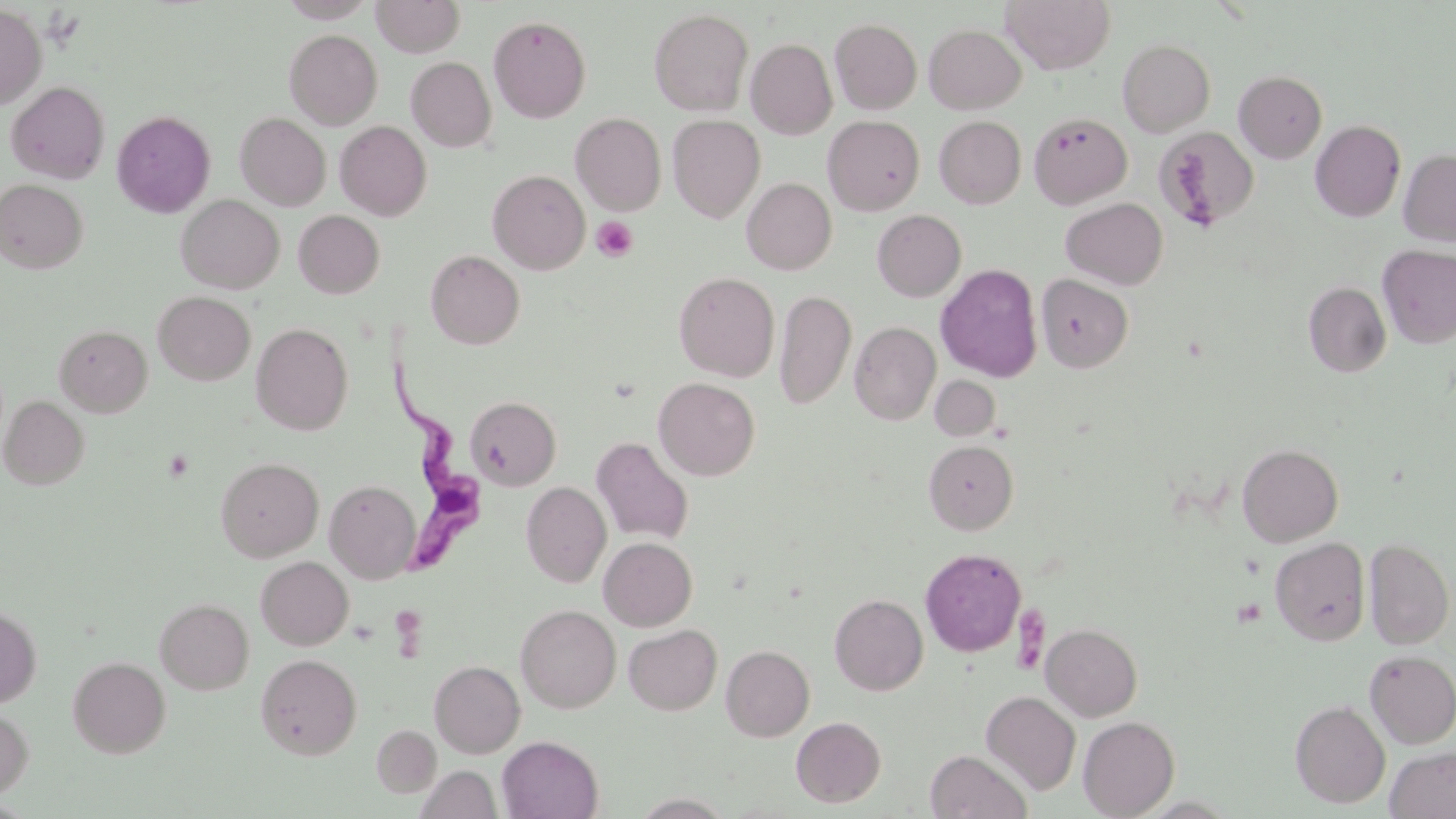
Summary:
  - Coordinate format: approximate bounding boxes as (x1,y1)-(x2,y2) corner pairs in pixels
  - Platelet locations: (591,216)-(638,262), (162,450)-(195,482), (1232,598)-(1266,627)
  - Uninfected red blood cell locations: (279,0)-(376,22), (371,0)-(465,57), (1001,0)-(1115,74), (0,4)-(46,110), (649,8)-(753,116), (489,15)-(591,123), (830,18)-(922,114), (924,24)-(1026,114), (285,29)-(382,129), (746,38)-(837,139), (1118,38)-(1215,137), (406,57)-(496,152), (1233,70)-(1327,163), (6,81)-(110,183), (112,110)-(216,218), (235,112)-(330,211), (571,112)-(667,216), (1029,112)-(1131,207), (667,115)-(766,222), (823,115)-(925,215), (934,116)-(1026,208), (1311,120)-(1406,221), (336,121)-(432,220), (1154,126)-(1258,232), (1398,148)-(1456,247), (488,170)-(590,274), (741,177)-(837,274), (1,179)-(88,273), (176,195)-(285,293), (1060,197)-(1167,289), (872,209)-(966,301), (293,210)-(385,298), (1377,244)-(1456,348), (426,249)-(524,349), (935,263)-(1042,382), (674,271)-(780,382), (1036,274)-(1133,373), (1304,282)-(1391,377), (774,289)-(856,410), (153,291)-(255,385), (849,321)-(941,425), (251,323)-(353,435), (54,324)-(152,417), (929,375)-(1001,441), (653,377)-(760,481), (0,395)-(89,490), (465,396)-(561,490), (592,436)-(694,545), (924,440)-(1019,534), (1237,443)-(1343,547), (215,457)-(324,562), (324,480)-(421,583), (521,482)-(612,587), (1270,536)-(1370,646), (1364,536)-(1454,649), (599,537)-(697,631), (920,548)-(1026,657), (256,556)-(354,650), (829,593)-(928,695), (155,598)-(254,695), (516,604)-(621,713), (0,605)-(41,708), (1041,623)-(1142,721), (623,624)-(722,715), (721,645)-(815,741), (1364,650)-(1456,748), (255,653)-(363,759), (67,656)-(170,757), (429,660)-(525,757), (981,691)-(1081,795), (1290,700)-(1391,808), (0,707)-(33,798), (791,716)-(886,807), (1078,716)-(1180,818), (371,725)-(441,797), (497,735)-(603,819), (1385,746)-(1456,819), (925,750)-(1033,819), (417,765)-(501,819)
  - Trypanosoma brucei locations: (381,362)-(492,581)
  - Slide-level diagnosis: Trypanosoma brucei
  - Preparation: thin blood film
  - Magnification: 1000x
  - Stain: May-Grünwald-Giemsa
  - Field of view: single
  - Modality: optical microscopy
  - Image size: 1456×819 pixels